Report the malaria status of this cell.
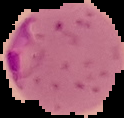

It is parasitized.

Summary:
  - Image type: segmented cell region with the area outside set to black
  - Image size: 124×118 pixels
  - Preparation: thin blood smear